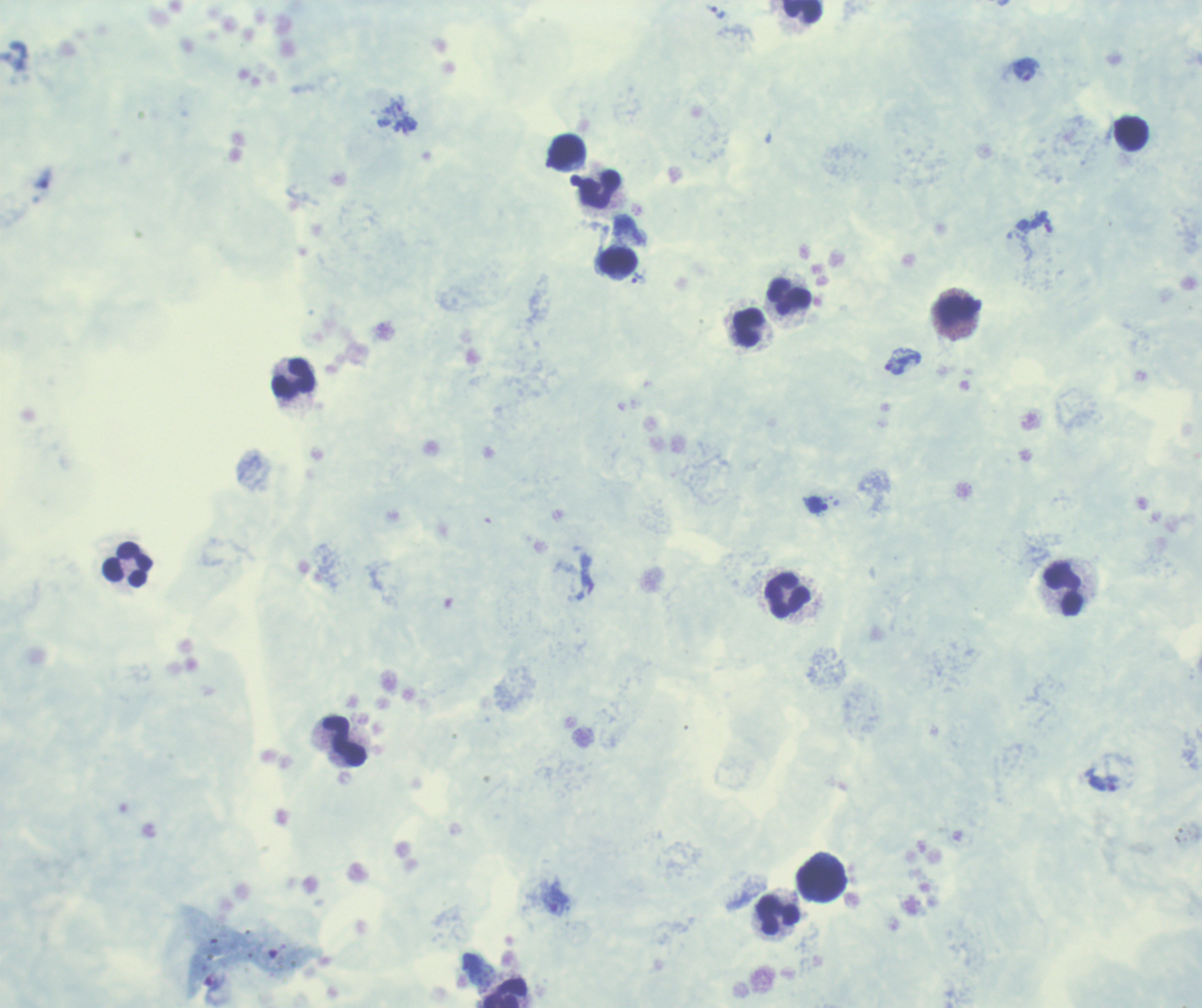
Approximate object centers, in pixels from the top-left corner. Trophozoite locations: (x=1025, y=69), (x=394, y=106), (x=638, y=278), (x=902, y=364), (x=816, y=505), (x=556, y=902). Leukocyte locations: (x=801, y=11), (x=1131, y=133), (x=567, y=151), (x=600, y=189), (x=618, y=261), (x=789, y=297), (x=959, y=310), (x=748, y=326), (x=294, y=378), (x=128, y=564), (x=1064, y=588), (x=788, y=596), (x=344, y=740), (x=822, y=879), (x=778, y=915), (x=506, y=993). Captured at 100x magnification. Romanowsky-stained preparation. Result: positive for malaria parasites. Single field of view. Background quality: unsatisfactory. Previously used in an actual diagnosis. Thick smear of blood. Image is 1202×1008 pixels.